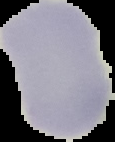
Image is 115×142 pixels. Segmented cell region on a black background. Result: negative for Plasmodium parasites. From a thin blood smear.